Locate and identify every blood parasite.
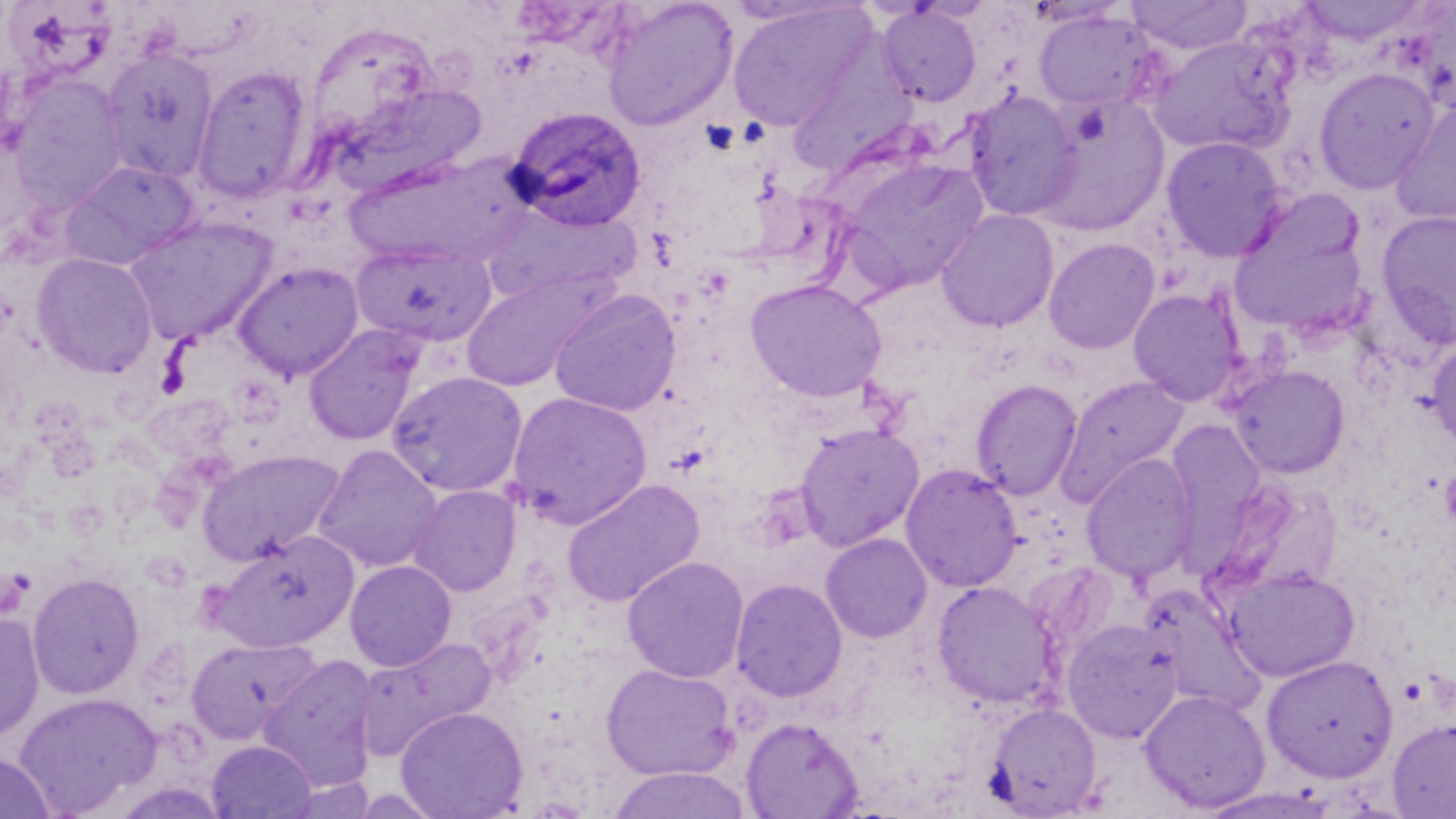
Approximate bounding boxes as [x1, y1, x2, y2] in pixels.
Plasmodium ovale-infected red blood cells: [506, 106, 647, 231].
No Plasmodium falciparum, Plasmodium malariae, Plasmodium vivax, Babesia divergens, or Trypanosoma brucei observed.

Summary:
  - Uninfected red blood cell locations: [601, 0, 738, 131], [1124, 0, 1252, 55], [727, 3, 872, 131], [878, 4, 981, 107], [1032, 8, 1161, 112], [304, 21, 441, 144], [1147, 35, 1294, 155], [100, 48, 218, 184], [192, 65, 313, 203], [1313, 67, 1441, 194], [9, 76, 129, 211], [333, 84, 488, 195], [963, 89, 1083, 222], [1032, 95, 1169, 237], [1390, 100, 1456, 228], [1161, 136, 1288, 262], [346, 152, 533, 269], [841, 157, 989, 293], [61, 160, 198, 270], [485, 202, 640, 307], [935, 208, 1059, 333], [1375, 209, 1456, 349], [124, 216, 276, 345], [1229, 221, 1369, 336], [1044, 237, 1160, 354], [351, 241, 496, 348], [31, 253, 156, 378], [232, 262, 364, 380], [458, 269, 608, 392], [746, 278, 887, 403], [549, 288, 681, 416], [1128, 288, 1246, 407], [303, 325, 425, 446], [1427, 337, 1456, 452], [1228, 365, 1350, 479], [387, 370, 528, 496], [1055, 375, 1190, 507], [971, 379, 1082, 500], [506, 391, 652, 528], [1166, 418, 1268, 540], [794, 422, 924, 551], [312, 444, 443, 573], [196, 450, 343, 565], [1081, 453, 1199, 585], [900, 463, 1023, 592], [561, 478, 705, 608], [408, 484, 522, 596], [211, 531, 358, 653], [820, 533, 933, 643], [622, 555, 749, 683], [344, 560, 457, 671], [1225, 567, 1359, 682], [27, 571, 145, 699], [730, 578, 847, 702], [931, 581, 1060, 710], [1140, 585, 1266, 716], [0, 611, 44, 745], [1061, 618, 1184, 743], [357, 635, 495, 759], [185, 636, 319, 745], [258, 654, 379, 791], [1261, 654, 1398, 782], [601, 663, 737, 780], [1139, 688, 1271, 813], [14, 693, 161, 816], [985, 702, 1102, 817], [395, 706, 528, 819], [740, 717, 863, 818], [1387, 717, 1456, 818], [207, 740, 316, 819], [0, 753, 57, 819], [606, 767, 751, 819]
  - Platelet locations: [1440, 469, 1456, 524]
  - Slide-level diagnosis: Plasmodium ovale
  - Preparation: thin blood smear
  - Field of view: single
  - Magnification: 1000x
  - Modality: optical microscopy
  - Image size: 1456×819 pixels
  - Stain: May-Grünwald-Giemsa